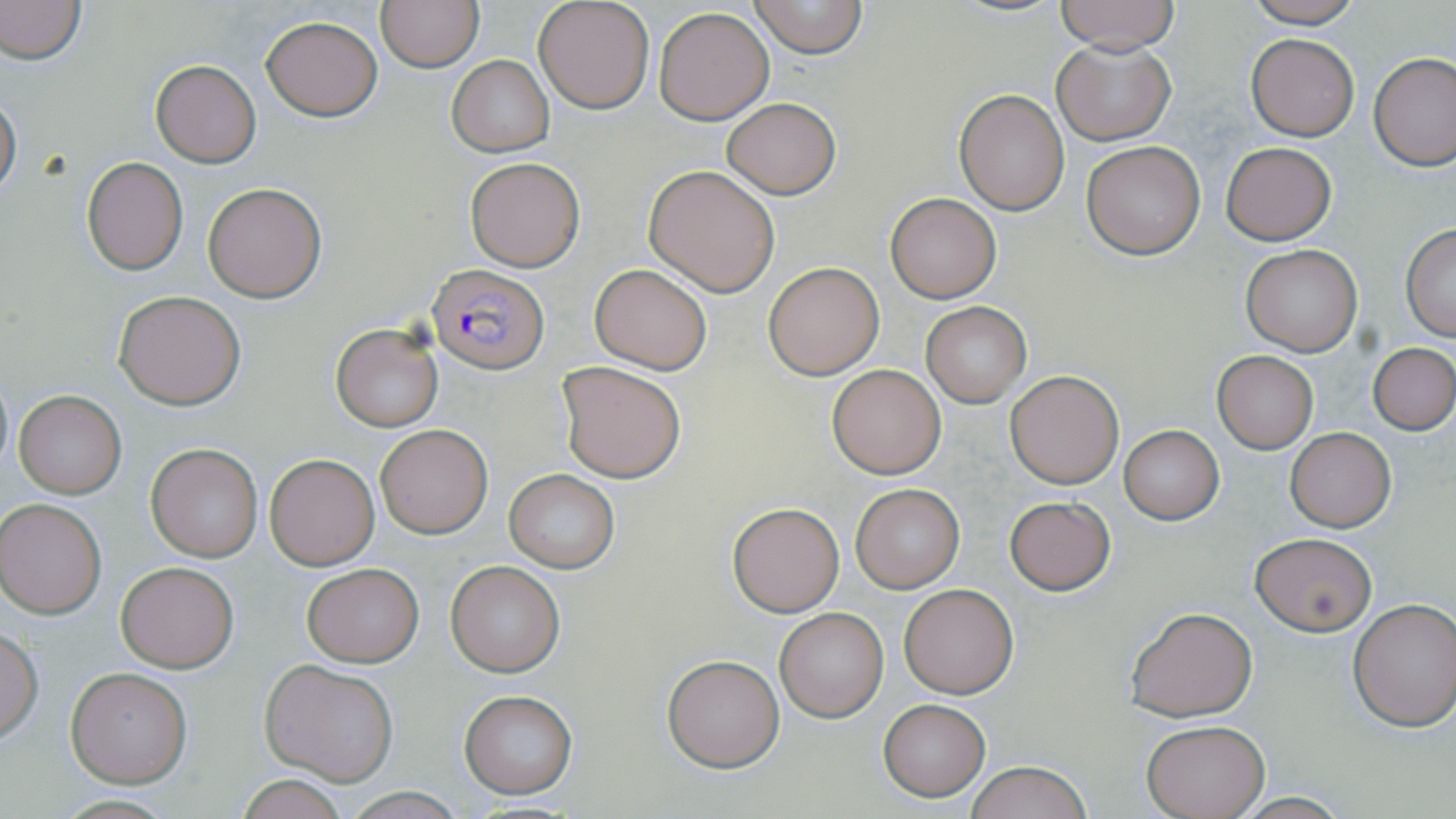
Approximate bounding boxes as (x1, y1, x2, y2) in pixels. Plasmodium falciparum-infected red blood cell locations: (428, 263, 549, 374). Uninfected red blood cell locations: (0, 0, 86, 65), (533, 0, 656, 115), (1053, 0, 1181, 53), (1237, 0, 1370, 28), (377, 1, 483, 72), (747, 1, 869, 59), (653, 6, 774, 125), (260, 14, 383, 121), (1246, 34, 1359, 140), (1052, 37, 1175, 145), (1369, 52, 1455, 170), (447, 56, 554, 155), (151, 61, 261, 168), (955, 89, 1070, 214), (0, 90, 21, 203), (722, 98, 840, 199), (1081, 140, 1205, 260), (1221, 141, 1336, 246), (82, 156, 187, 275), (464, 156, 584, 272), (644, 164, 781, 296), (202, 182, 327, 301), (886, 193, 1001, 303), (1401, 224, 1455, 340), (1241, 245, 1363, 357), (763, 261, 884, 380), (589, 264, 712, 375), (113, 290, 247, 410), (921, 302, 1031, 408), (331, 323, 443, 431), (1369, 342, 1456, 434), (1210, 350, 1320, 454), (556, 360, 686, 483), (825, 363, 946, 479), (0, 367, 12, 481), (1004, 369, 1124, 489), (13, 391, 126, 498), (375, 424, 493, 538), (1119, 425, 1223, 525), (1285, 427, 1397, 532), (146, 443, 264, 562), (264, 454, 380, 571), (505, 468, 620, 573), (851, 484, 964, 593), (1005, 496, 1115, 595), (1, 498, 106, 618), (727, 501, 844, 617), (1251, 533, 1376, 634), (445, 560, 566, 677), (115, 561, 239, 672), (301, 563, 424, 666), (897, 582, 1019, 699), (1348, 599, 1456, 731), (1125, 605, 1259, 721), (775, 607, 888, 721), (0, 625, 44, 745), (661, 653, 786, 773), (261, 659, 399, 784), (65, 667, 192, 787), (457, 689, 578, 799), (878, 699, 990, 800), (1141, 719, 1271, 819), (964, 760, 1094, 819), (232, 775, 353, 818). Slide-level diagnosis: Plasmodium falciparum. Thin blood film. Single field of view. Image is 1456×819 pixels. May-Grünwald-Giemsa-stained preparation. 1000x magnification. Optical microscopy.